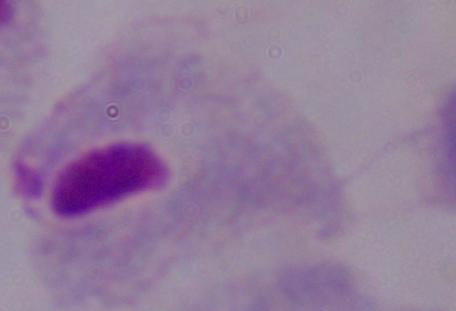 Captured at 1000x magnification. Photomicrograph. A trichomonad is seen.